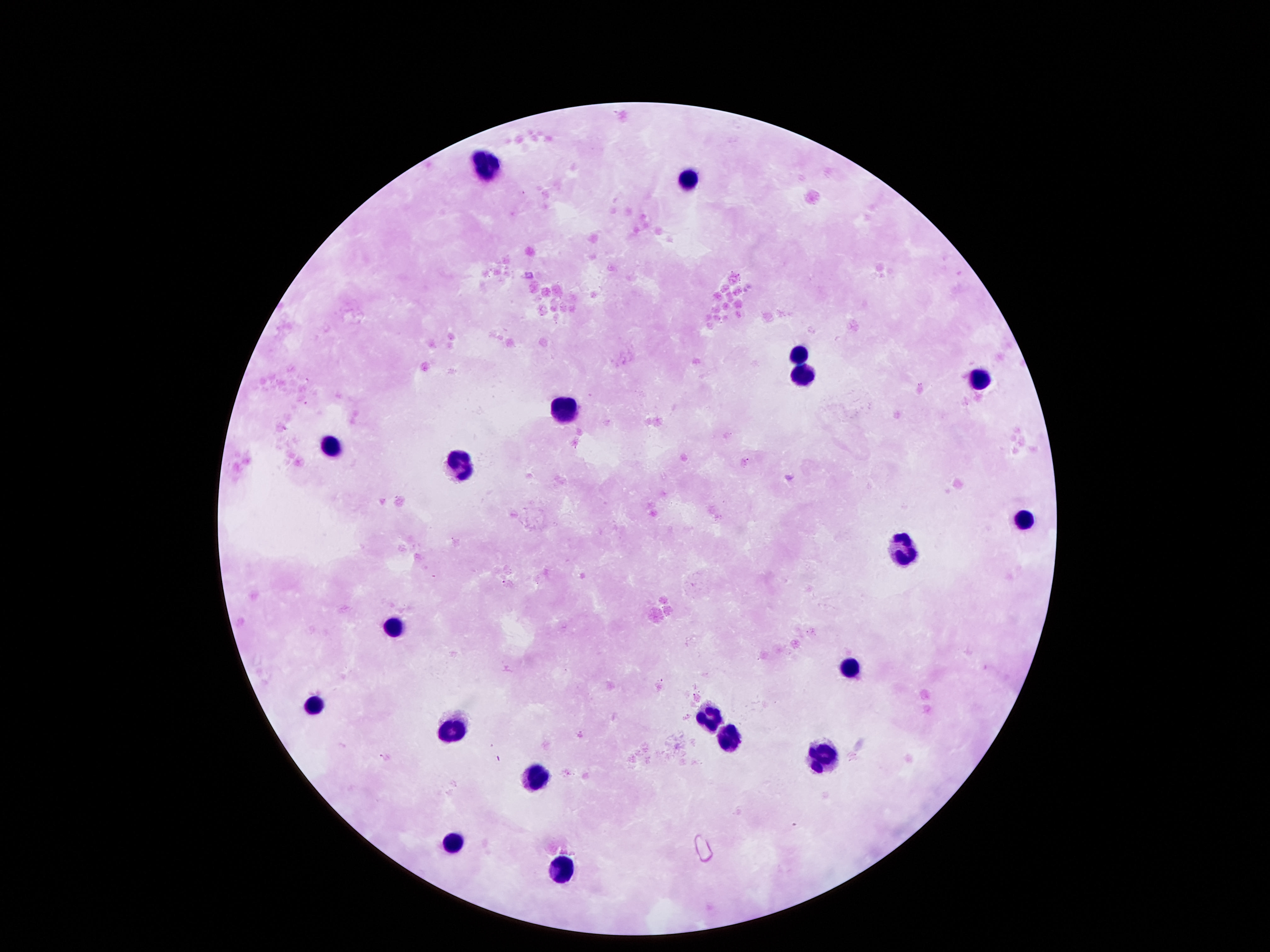

{
  "stain": "Giemsa",
  "patient_malaria_status": "negative",
  "preparation": "thick blood smear",
  "leukocyte_locations": "approximate centers as (x, y) in pixels: (487, 162), (685, 179), (799, 351), (803, 374), (981, 381), (567, 411), (332, 445), (463, 458), (1025, 519), (907, 548), (396, 623), (850, 663), (308, 704), (709, 710), (453, 731), (729, 734), (823, 758), (540, 778), (450, 838), (557, 868)",
  "capture": "smartphone camera through the microscope eyepiece",
  "image_size": "1270×952 pixels",
  "field_of_view": "one from this slide",
  "magnification": "100x"
}